Classify this cell by malaria status.
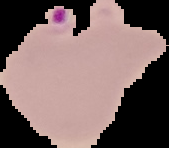

Parasitized.

Summary:
  - Preparation: thin blood film
  - Image type: segmented cell region on a black background
  - Image size: 169×148 pixels